Classify this cell by malaria status.
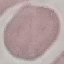
It is uninfected.

Summary:
  - Image type: automatically extracted cell patch, resized to 64 × 64 pixels
  - Preparation: thin smear
  - Stain: Giemsa
  - Capture: smartphone through the microscope eyepiece